Give the position of every Plasmodium parasite and every leukocyte.
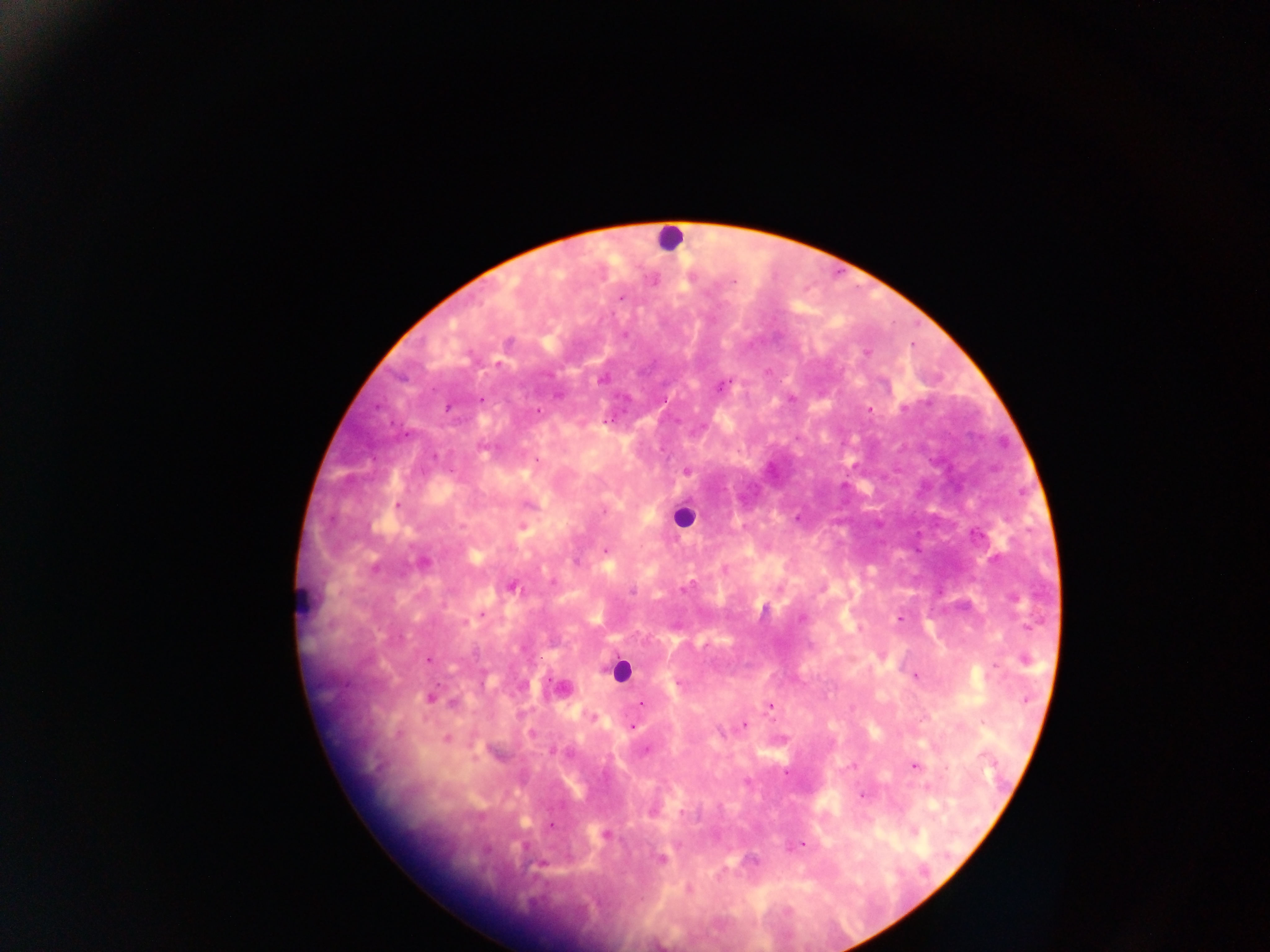

Approximate centers as x y in pixels.
Plasmodium parasites: 621 298; 625 334; 508 342; 866 352; 602 380; 721 387; 558 395; 481 399; 448 409; 869 409; 538 411; 606 421; 687 471; 398 505; 604 511; 522 526; 605 550; 423 562; 575 562; 724 570; 512 586; 684 588; 632 591; 764 610; 482 614; 802 618; 899 618; 429 660; 1025 660; 916 676; 679 683; 1027 698; 430 699; 452 704; 642 704; 770 707; 593 716; 745 725; 633 726; 446 738; 647 749; 554 751; 915 766; 785 773; 927 788; 861 794; 681 813; 551 826; 605 834; 802 844; 661 859.
Leukocytes: 670 237; 683 517; 304 597; 620 671.

capture = mobile-phone photograph through a microscope
image size = 1270×952 pixels
country = Ghana
field of view = single
preparation = thick blood smear